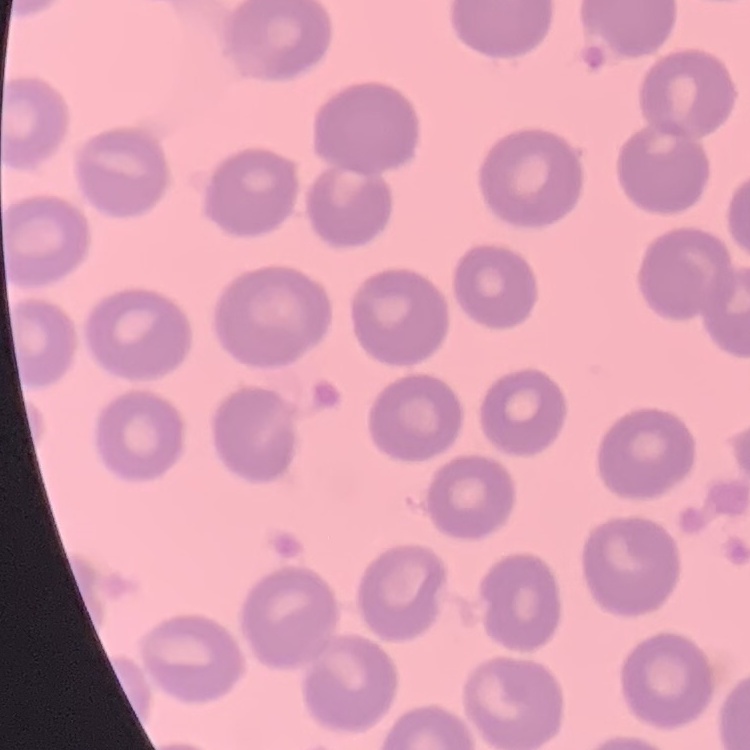
Summary:
  - Erythrocyte morphology: no rouleaux formation
  - Stain: Field's or Giemsa
  - Preparation: thin blood film
  - Image type: square crop of a larger photomicrograph